Mark where platelets are.
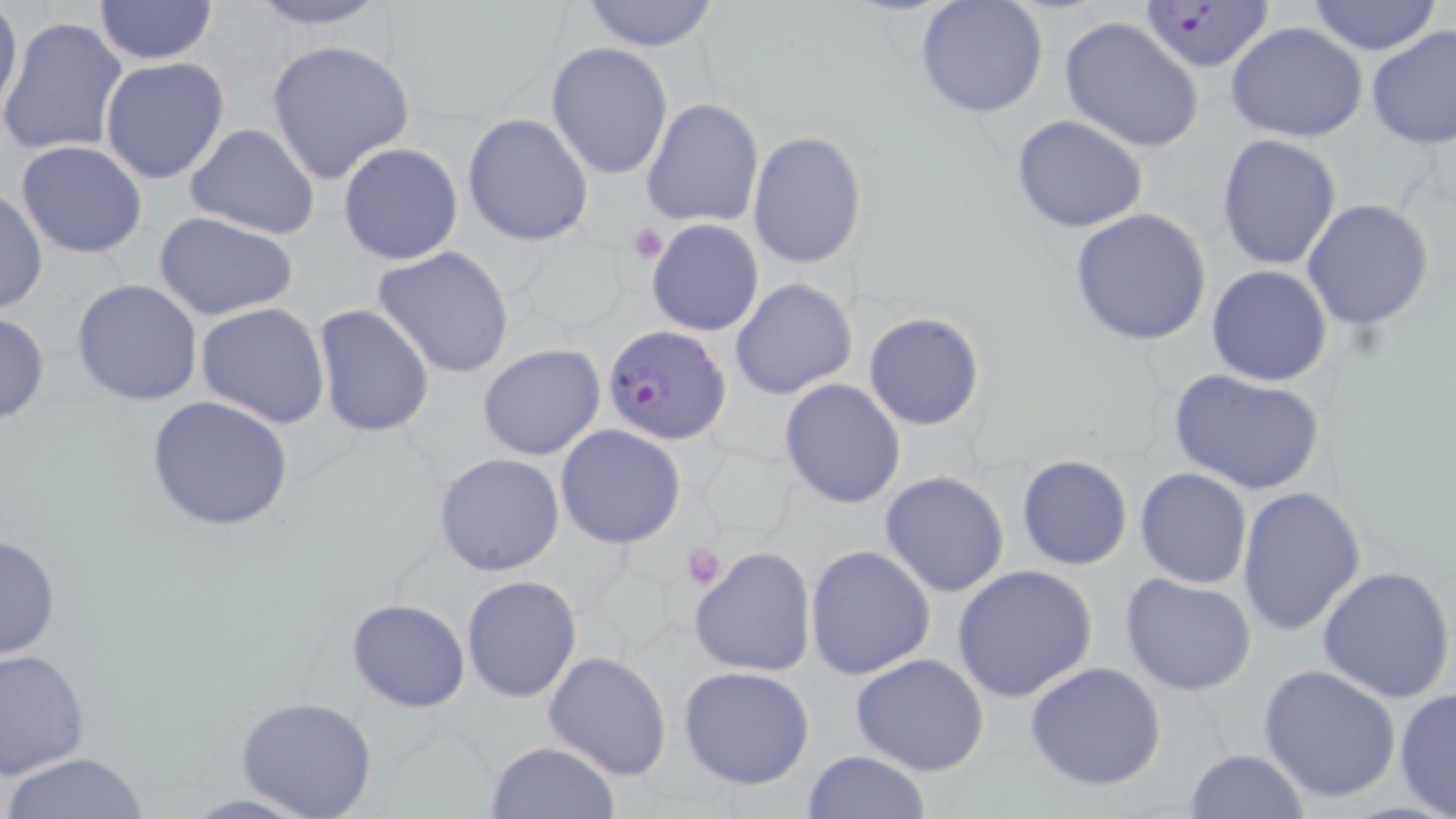
Approximate bounding boxes as (x1,y1)-(x2,y2) corner pairs in pixels.
Platelets: (627,222)-(668,264), (682,543)-(727,590).

Summary:
  - Uninfected red blood cell locations: (242,0)-(396,30), (577,0)-(724,51), (914,0)-(1050,120), (1304,0)-(1445,55), (1,1)-(24,116), (92,1)-(218,66), (1058,15)-(1206,154), (0,17)-(131,160), (1225,21)-(1368,143), (1366,25)-(1456,152), (265,39)-(416,184), (545,43)-(674,180), (100,56)-(230,184), (642,98)-(764,229), (462,112)-(594,247), (1010,115)-(1149,235), (185,123)-(321,240), (747,131)-(868,270), (1215,133)-(1343,270), (15,140)-(148,258), (338,142)-(463,266), (0,187)-(48,316), (1301,198)-(1435,331), (1069,208)-(1213,345), (152,212)-(302,322), (645,218)-(764,337), (373,247)-(514,379), (1207,265)-(1331,387), (730,277)-(858,401), (72,279)-(203,407), (197,303)-(330,428), (313,303)-(436,437), (0,309)-(50,425), (864,313)-(984,429), (477,345)-(605,461), (1172,371)-(1323,498), (779,378)-(907,508), (145,395)-(296,531), (555,425)-(687,550), (433,453)-(565,577), (1016,455)-(1134,571), (1135,468)-(1252,589), (879,471)-(1010,597), (1236,487)-(1367,637), (0,532)-(61,661), (689,545)-(817,678), (805,545)-(935,682), (951,564)-(1100,704), (1315,565)-(1456,705), (461,574)-(583,703), (1119,574)-(1258,696), (347,597)-(470,712), (1,649)-(90,778), (543,650)-(673,780), (849,653)-(991,775), (1025,661)-(1168,792), (1258,663)-(1401,803), (678,665)-(817,790), (1394,689)-(1456,818), (235,695)-(379,819), (484,740)-(620,819), (1184,747)-(1310,819), (800,749)-(931,819), (2,751)-(152,819)
  - Plasmodium falciparum-infected red blood cell locations: (1137,0)-(1277,74), (602,325)-(732,445)
  - Slide-level diagnosis: Plasmodium falciparum
  - Image size: 1456×819 pixels
  - Modality: optical microscopy
  - Stain: May-Grünwald-Giemsa
  - Magnification: 1000x
  - Field of view: single
  - Preparation: thin blood smear